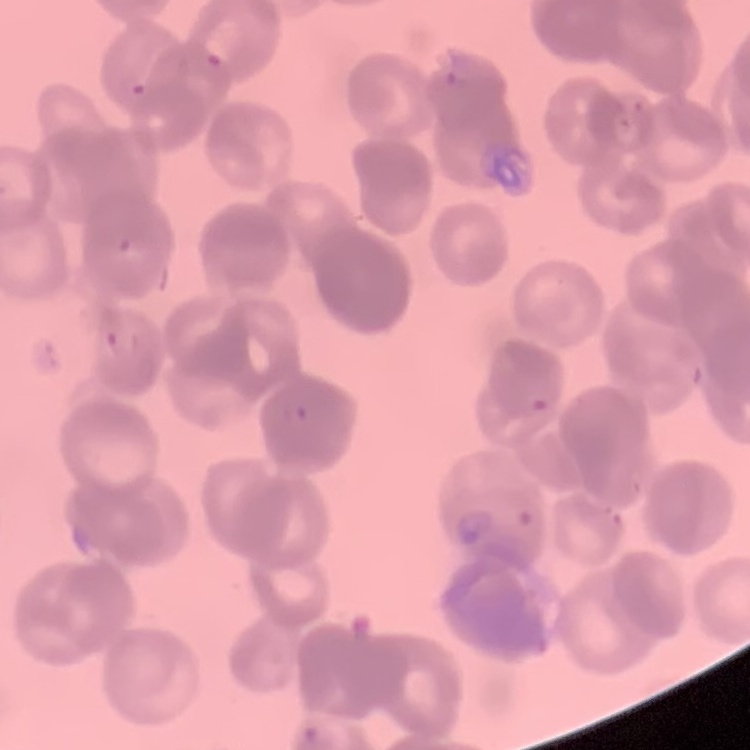

Summary:
  - Red blood cell morphology: rouleaux formation
  - Image type: one tile cut from a larger photomicrograph
  - Stain: Field's or Giemsa
  - Preparation: thin blood film